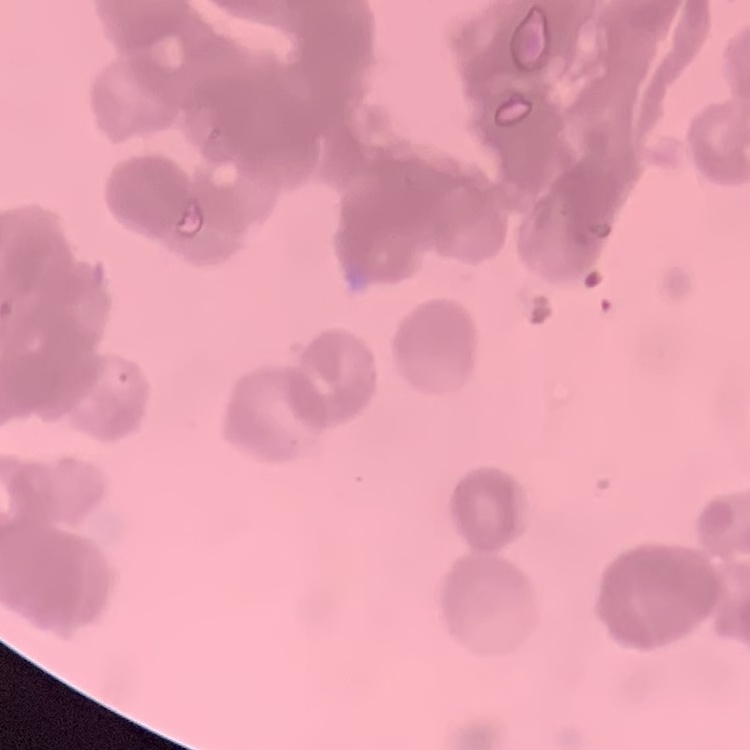
The erythrocytes show rouleaux formation. Stained with either Field's or Giemsa. Thin blood smear. One tile cut from a larger photomicrograph.